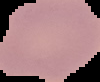
{
  "image_type": "segmented cell region with the area outside set to black",
  "preparation": "thin blood film",
  "result": "negative for malaria parasites",
  "image_size": "100×82 pixels"
}